Give the preparation type.
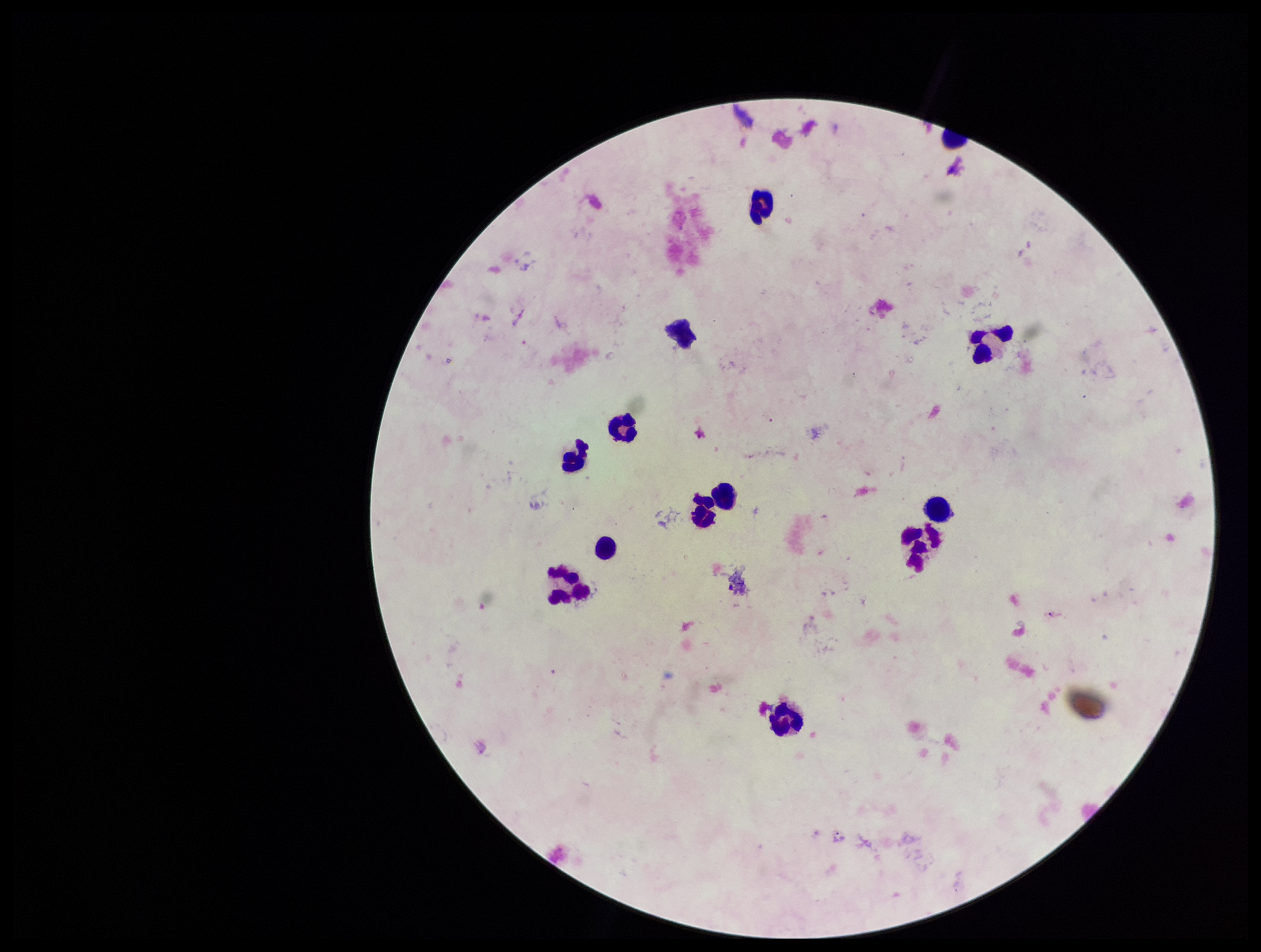
Thick.

patient_malaria_status: negative
field_of_view: single
image_size: 1261×952 pixels
leukocyte_count: 13
plasmodium_parasites: none detected
capture: smartphone photograph through the microscope eyepiece
parasite_count: 0
stain: Giemsa